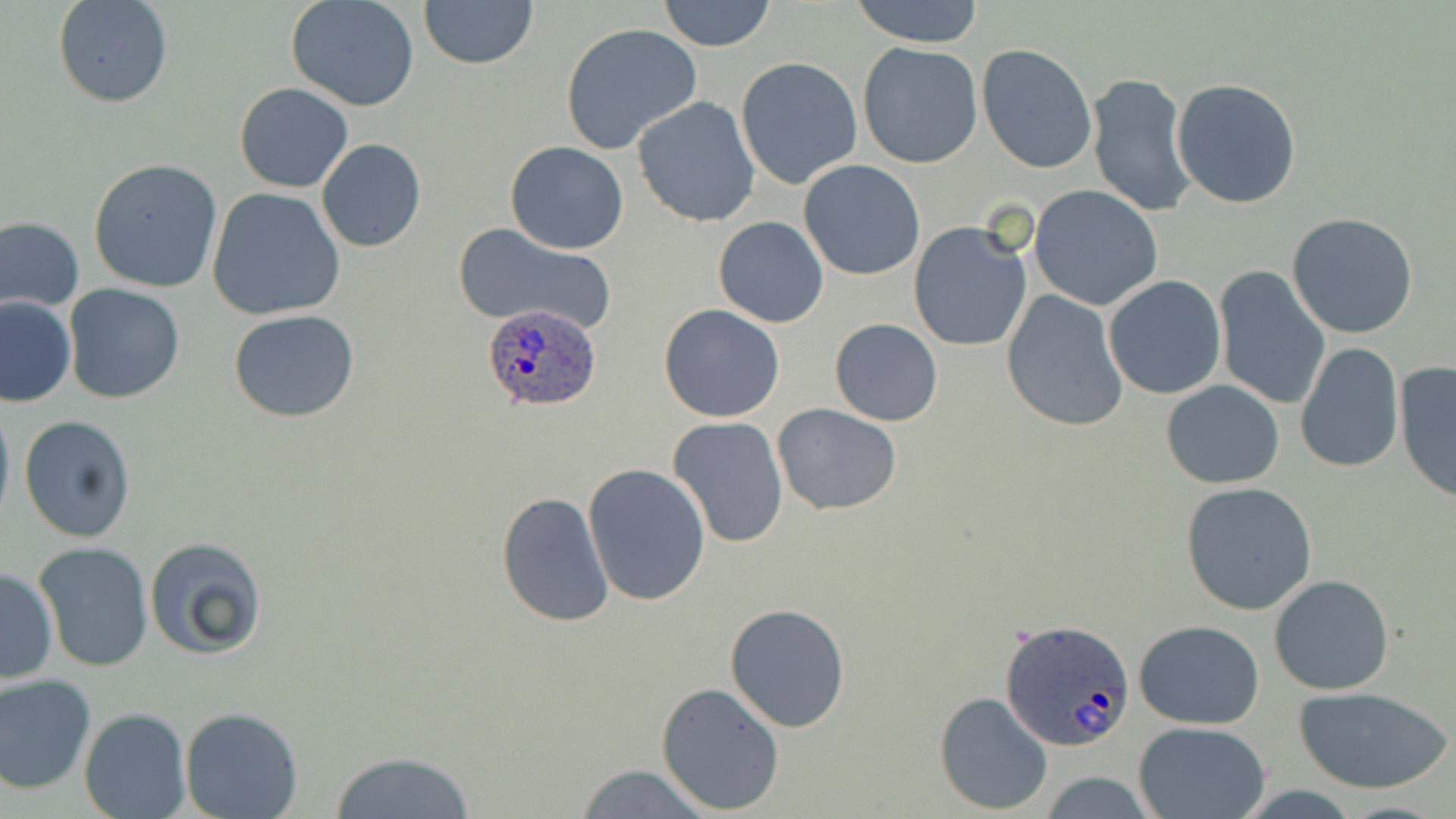

slide_level_diagnosis: Plasmodium ovale
stain: May-Grünwald-Giemsa
image_size: 1456×819 pixels
uninfected_red_blood_cell_locations: 'approximate bounding boxes as (x1, y1, x2, y2) in pixels: (53, 0, 173, 108), (287, 0, 420, 112), (418, 0, 539, 71), (657, 0, 776, 51), (851, 0, 986, 48), (559, 22, 702, 154), (977, 43, 1099, 175), (857, 44, 983, 168), (735, 56, 863, 191), (1086, 71, 1198, 218), (1171, 79, 1303, 209), (235, 82, 352, 193), (631, 96, 763, 227), (316, 139, 427, 253), (505, 141, 628, 254), (88, 159, 222, 293), (799, 160, 926, 280), (1030, 185, 1162, 311), (207, 187, 347, 320), (1286, 212, 1421, 339), (713, 215, 830, 328), (1, 217, 84, 314), (908, 221, 1033, 353), (454, 225, 618, 335), (1215, 266, 1331, 410), (1102, 275, 1227, 399), (63, 284, 184, 403), (1001, 289, 1130, 431), (1, 297, 75, 407), (658, 304, 785, 422), (229, 310, 361, 423), (829, 319, 943, 426), (1295, 343, 1403, 472), (1394, 362, 1455, 505), (1161, 380, 1285, 489), (0, 396, 14, 531), (772, 403, 904, 516), (18, 414, 136, 542), (665, 415, 789, 549), (583, 463, 711, 606), (1179, 481, 1319, 614), (497, 492, 615, 628), (143, 536, 268, 660), (34, 542, 153, 673), (0, 567, 58, 684), (1268, 573, 1396, 695), (724, 603, 850, 732), (1134, 619, 1265, 729), (0, 673, 96, 795), (655, 681, 785, 814), (1294, 687, 1452, 795), (934, 691, 1053, 812), (78, 705, 191, 819), (180, 708, 305, 819), (1133, 721, 1273, 819), (329, 750, 476, 819), (574, 763, 713, 818), (1037, 772, 1164, 818)'
field_of_view: single
preparation: thin blood film
plasmodium_ovale_infected_red_blood_cell_locations: 'approximate bounding boxes as (x1, y1, x2, y2) in pixels: (476, 305, 606, 416), (1000, 616, 1136, 752)'
modality: light microscopy
magnification: 1000x